Assess this cell for malaria.
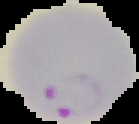
It is parasitized.

Summary:
  - Image type: cell region segmented out of the field of view; surrounding area masked to black
  - Preparation: thin blood film
  - Image size: 139×124 pixels